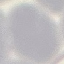
malaria status = uninfected
preparation = thin blood smear
capture = smartphone camera at the microscope eyepiece
stain = Giemsa
image type = automatically extracted cell patch, resized to 64 × 64 pixels